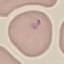

Summary:
  - Result: malaria parasites detected
  - Capture: smartphone through the microscope eyepiece
  - Stain: Giemsa
  - Preparation: thin smear
  - Image type: cell patch, automatically extracted from a larger field of view and resized to 64 × 64 pixels